Locate every leukocyte (white blood cell).
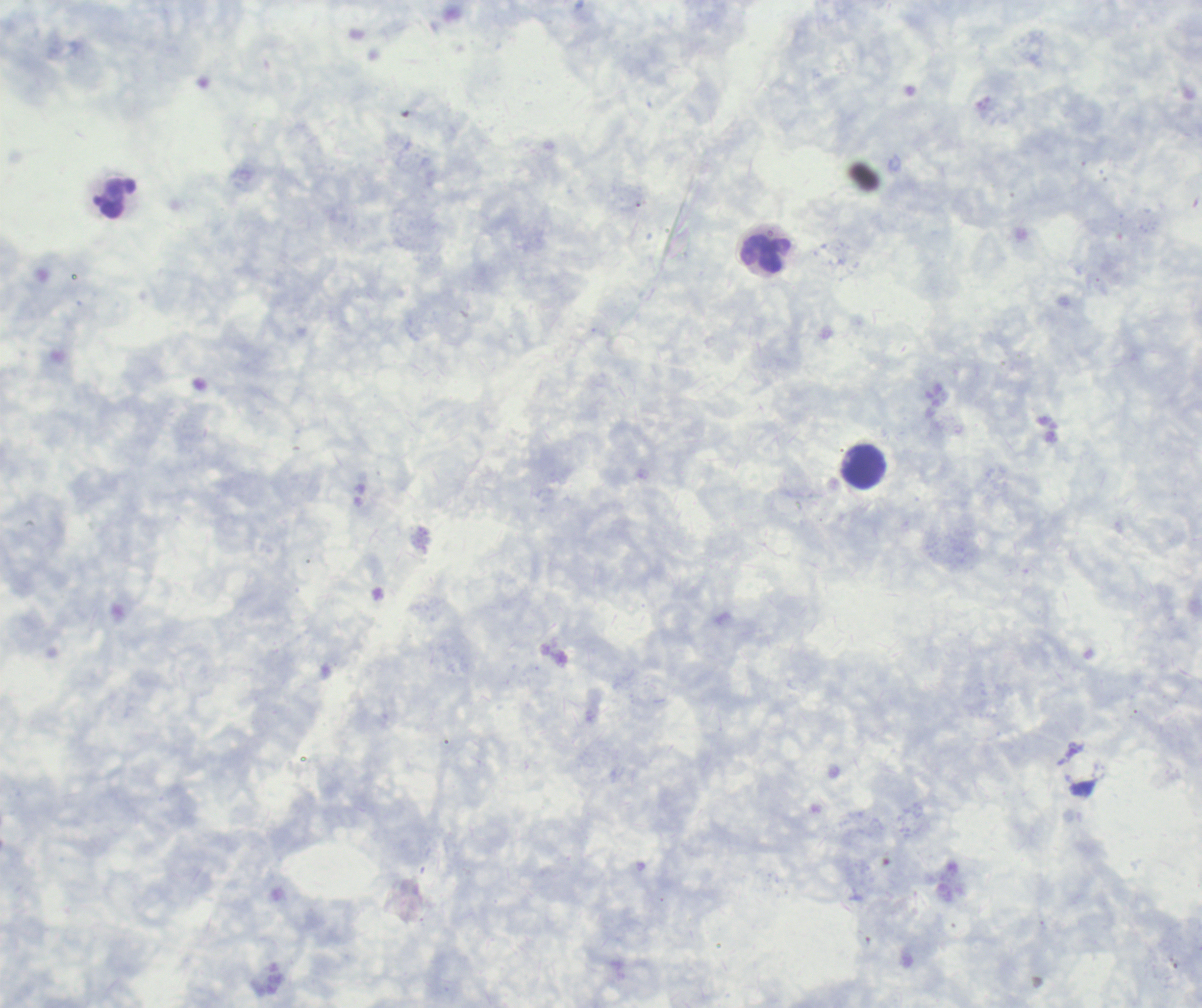
Approximate centers as [x, y] in pixels.
Leukocytes: [117, 200], [767, 253], [864, 467].

Romanowsky stain. Background quality: poor. Thick blood film. Single field of view. Coloration quality: good. Image is 1202×1008 pixels. Captured at 100x magnification. Previously used in an actual diagnosis. Result: no malaria parasites detected.